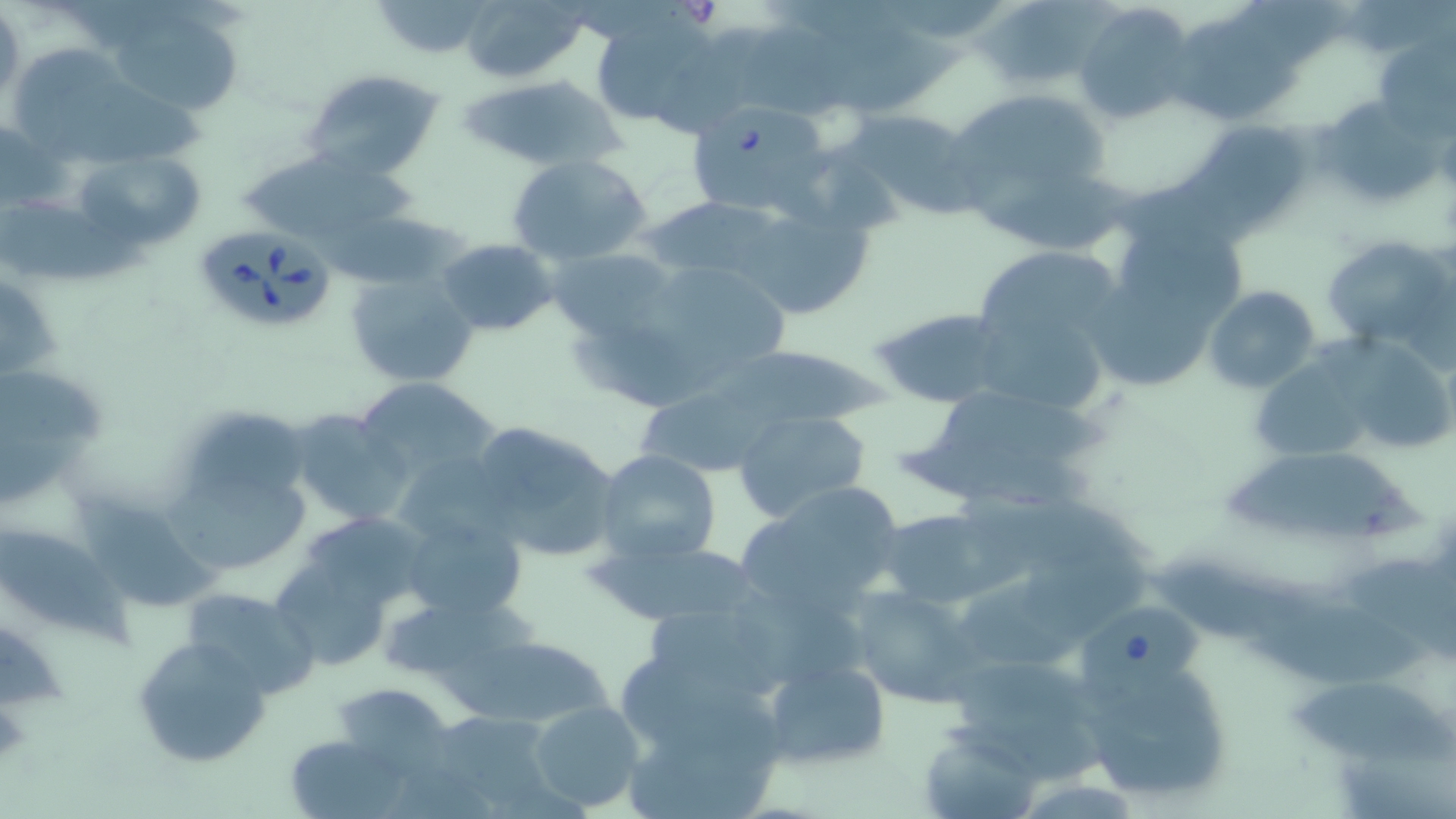

Summary:
  - Coordinate format: approximate bounding boxes as (x1, y1, x2, y2) in pixels
  - Uninfected red blood cell locations: (369, 0, 498, 55), (100, 1, 246, 117), (970, 1, 1132, 91), (472, 2, 597, 83), (1076, 4, 1198, 125), (1, 5, 26, 110), (586, 8, 736, 134), (816, 24, 968, 109), (1174, 26, 1305, 124), (1381, 42, 1455, 146), (301, 68, 448, 183), (460, 72, 624, 174), (18, 78, 214, 162), (941, 88, 1114, 233), (1330, 103, 1449, 204), (843, 108, 985, 219), (1182, 122, 1318, 234), (237, 147, 422, 251), (74, 149, 204, 249), (506, 154, 653, 267), (643, 195, 793, 285), (726, 195, 880, 322), (1, 199, 154, 280), (1124, 224, 1258, 341), (1321, 234, 1453, 354), (438, 237, 559, 336), (544, 247, 679, 347), (976, 255, 1119, 353), (637, 257, 791, 368), (345, 267, 482, 386), (1090, 273, 1216, 395), (1204, 285, 1321, 395), (870, 306, 1008, 409), (567, 317, 740, 410), (1313, 333, 1451, 452), (714, 347, 894, 424), (0, 359, 105, 508), (1258, 364, 1381, 464), (354, 377, 502, 489), (905, 381, 1112, 513), (638, 396, 790, 478), (170, 403, 314, 517), (288, 409, 413, 527), (732, 409, 871, 523), (466, 418, 621, 563), (595, 450, 722, 565), (1214, 451, 1430, 541), (168, 453, 318, 581), (738, 481, 909, 616), (875, 506, 1003, 607), (402, 511, 528, 621), (0, 522, 122, 637), (272, 528, 418, 669), (588, 536, 762, 626), (1148, 557, 1336, 646), (1345, 557, 1456, 665), (1016, 564, 1159, 646), (847, 585, 981, 707), (178, 586, 321, 699), (1255, 600, 1434, 694), (0, 630, 69, 713), (452, 633, 619, 731), (132, 635, 273, 768), (1078, 651, 1234, 806), (946, 654, 1108, 778), (760, 657, 890, 771), (618, 659, 777, 750), (333, 682, 453, 773), (1289, 683, 1451, 761), (528, 701, 646, 812), (420, 709, 566, 815), (286, 733, 408, 817), (923, 737, 1039, 813)
  - Babesia divergens-infected red blood cell locations: (685, 100, 831, 218), (194, 224, 337, 335), (1068, 596, 1208, 704)
  - Slide-level diagnosis: Babesia divergens
  - Field of view: one of a larger specimen
  - Magnification: 1000x
  - Modality: optical microscopy
  - Image size: 1456×819 pixels
  - Preparation: thin blood film
  - Stain: May-Grünwald-Giemsa